Locate every Plasmodium parasite by life-cycle stage, and every leukocyte.
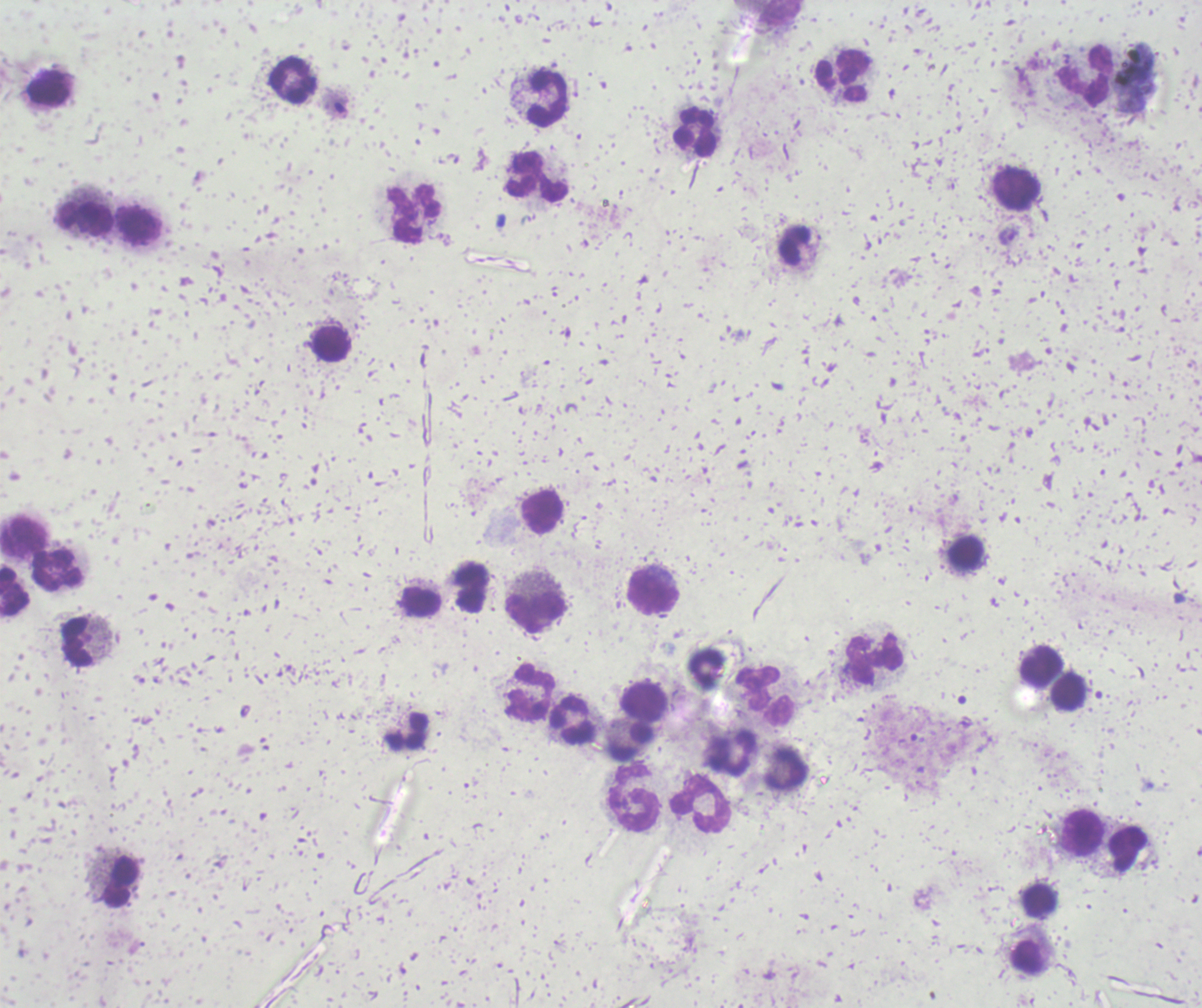

Approximate centers as (x, y) in pixels.
Trophozoites: (1007, 235).
No schizont or gametocyte forms observed.
Leukocytes: (781, 13), (841, 76), (1085, 76), (293, 81), (49, 87), (547, 97), (696, 131), (538, 177), (1017, 189), (413, 213), (85, 220), (138, 226), (795, 245), (331, 344), (542, 512), (23, 535), (966, 553), (57, 570), (471, 587), (14, 591), (653, 594), (421, 602), (535, 612), (79, 643), (876, 659), (1042, 667), (705, 669), (529, 691), (1069, 691), (765, 696), (645, 701), (573, 719), (407, 732), (630, 741), (731, 753), (785, 769), (634, 798), (701, 804), (1082, 832), (1128, 851), (121, 880), (1040, 900), (1028, 958).

Summary:
  - Magnification: 100x
  - Context: previously used in a real diagnosis
  - Image size: 1202×1008 pixels
  - Preparation: thick blood smear
  - Background quality: unsatisfactory
  - Stain: Romanowsky
  - Field of view: one from this slide